Name the blood parasite species.
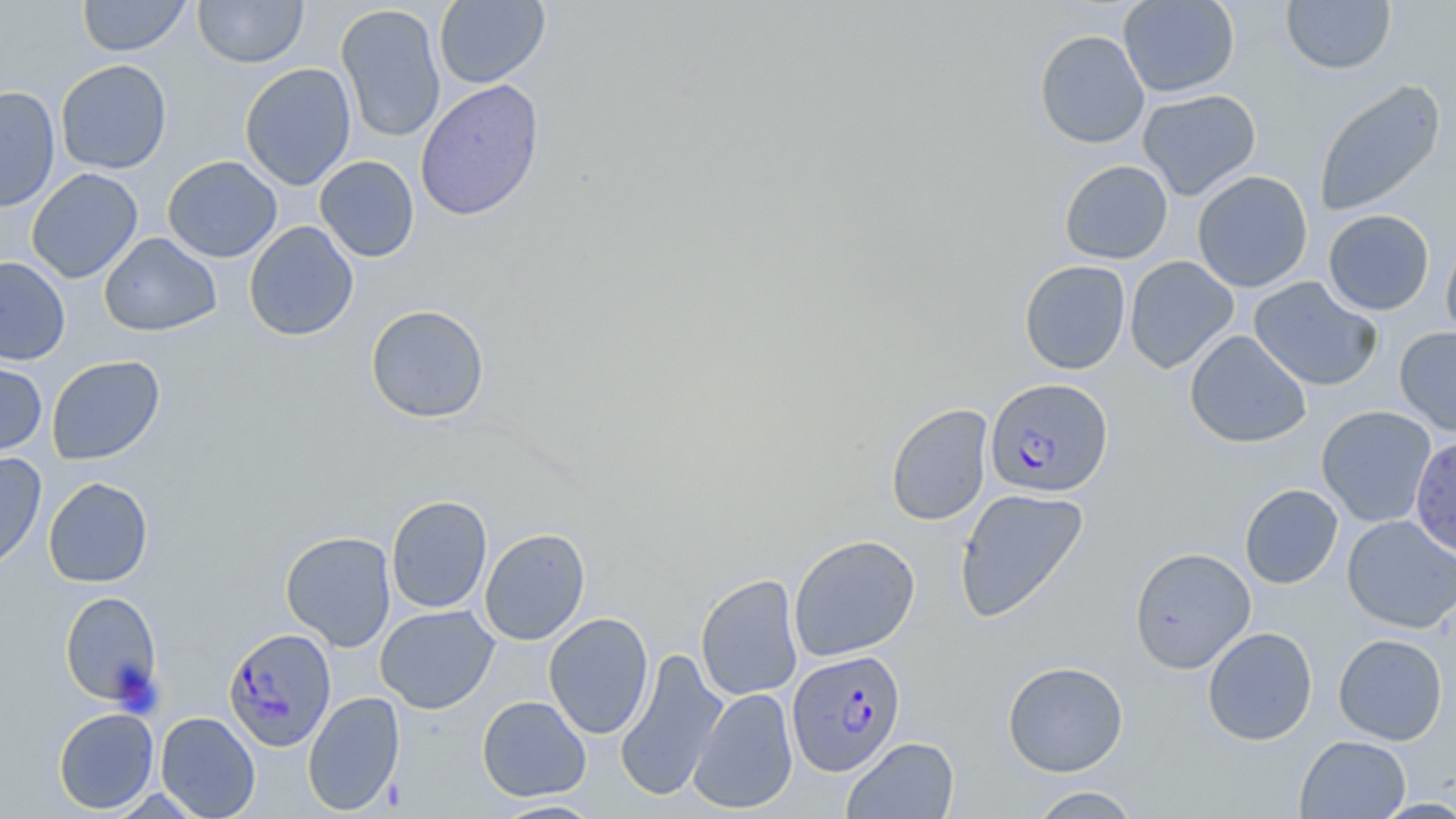

Plasmodium falciparum.

image_size: 1456×819 pixels
magnification: 1000x
modality: light microscopy
uninfected_red_blood_cell_locations: 'approximate bounding boxes as named x1/y1/x2/y2 corners in pixels: (x1=77, y1=0, x2=191, y2=57), (x1=193, y1=0, x2=308, y2=68), (x1=434, y1=0, x2=550, y2=89), (x1=1118, y1=0, x2=1239, y2=98), (x1=1281, y1=0, x2=1397, y2=75), (x1=336, y1=4, x2=446, y2=143), (x1=1034, y1=29, x2=1150, y2=149), (x1=55, y1=59, x2=172, y2=174), (x1=240, y1=63, x2=357, y2=191), (x1=415, y1=78, x2=544, y2=221), (x1=1313, y1=78, x2=1446, y2=217), (x1=0, y1=86, x2=61, y2=213), (x1=1137, y1=89, x2=1261, y2=201), (x1=162, y1=155, x2=283, y2=262), (x1=314, y1=156, x2=420, y2=262), (x1=1059, y1=160, x2=1173, y2=264), (x1=27, y1=168, x2=143, y2=283), (x1=1192, y1=170, x2=1313, y2=292), (x1=1323, y1=209, x2=1435, y2=315), (x1=243, y1=221, x2=359, y2=342), (x1=1440, y1=231, x2=1456, y2=343), (x1=99, y1=232, x2=222, y2=337), (x1=1124, y1=255, x2=1239, y2=374), (x1=0, y1=257, x2=70, y2=365), (x1=1019, y1=260, x2=1131, y2=375), (x1=1249, y1=276, x2=1382, y2=391), (x1=366, y1=304, x2=490, y2=423), (x1=1394, y1=326, x2=1456, y2=436), (x1=1184, y1=330, x2=1311, y2=449), (x1=46, y1=355, x2=165, y2=465), (x1=0, y1=358, x2=48, y2=458), (x1=885, y1=403, x2=994, y2=526), (x1=1316, y1=405, x2=1436, y2=527), (x1=1409, y1=433, x2=1456, y2=560), (x1=0, y1=452, x2=47, y2=575), (x1=43, y1=477, x2=153, y2=587), (x1=1239, y1=484, x2=1343, y2=589), (x1=954, y1=488, x2=1090, y2=623), (x1=386, y1=495, x2=492, y2=613), (x1=1342, y1=515, x2=1456, y2=634), (x1=479, y1=527, x2=590, y2=645), (x1=280, y1=531, x2=396, y2=651), (x1=789, y1=534, x2=920, y2=661), (x1=1129, y1=547, x2=1256, y2=674), (x1=695, y1=574, x2=804, y2=701), (x1=60, y1=590, x2=162, y2=707), (x1=375, y1=605, x2=499, y2=713), (x1=544, y1=612, x2=654, y2=739), (x1=1202, y1=626, x2=1318, y2=746), (x1=1333, y1=634, x2=1448, y2=745), (x1=614, y1=648, x2=729, y2=802), (x1=1002, y1=661, x2=1129, y2=777), (x1=688, y1=687, x2=798, y2=814), (x1=302, y1=691, x2=405, y2=815), (x1=477, y1=696, x2=591, y2=801), (x1=53, y1=707, x2=159, y2=814), (x1=156, y1=711, x2=260, y2=818), (x1=1295, y1=735, x2=1411, y2=819), (x1=842, y1=736, x2=959, y2=819), (x1=1027, y1=786, x2=1142, y2=818), (x1=1371, y1=797, x2=1456, y2=818), (x1=490, y1=798, x2=607, y2=818)'
plasmodium_falciparum_infected_red_blood_cell_locations: 'approximate bounding boxes as named x1/y1/x2/y2 corners in pixels: (x1=985, y1=379, x2=1113, y2=499), (x1=223, y1=627, x2=337, y2=751), (x1=786, y1=650, x2=905, y2=776)'
preparation: thin blood film
stain: May-Grünwald-Giemsa
field_of_view: single